Give the extent of all Trypanosoma brucei.
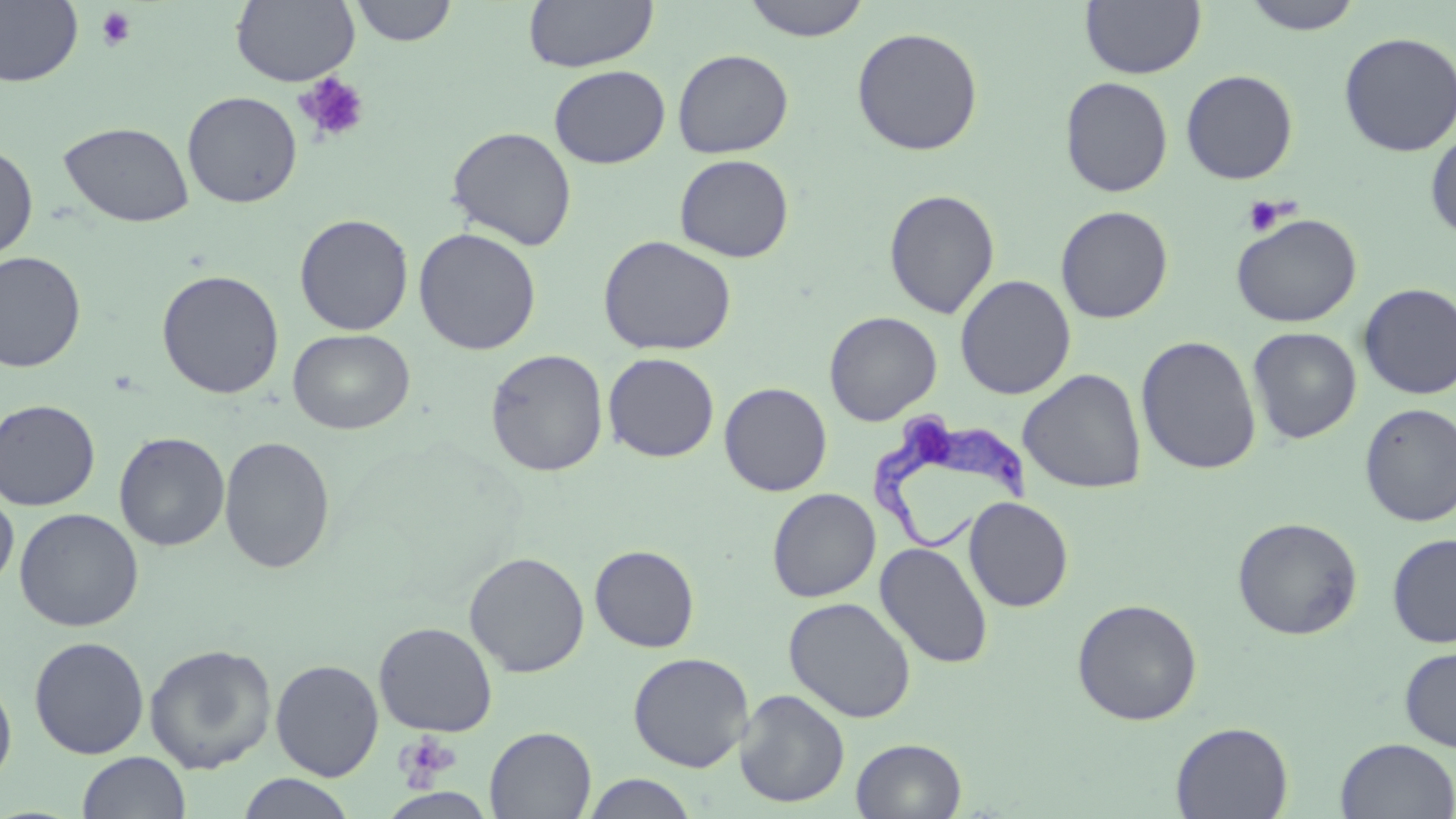
Approximate bounding boxes as (x1, y1, x2, y2) in pixels.
Trypanosoma brucei: (867, 413, 1041, 555).

Summary:
  - Uninfected red blood cell locations: (0, 0, 83, 87), (231, 0, 359, 86), (350, 0, 458, 46), (523, 0, 658, 73), (741, 0, 871, 41), (1079, 0, 1206, 79), (1239, 0, 1366, 35), (851, 26, 983, 156), (1338, 31, 1456, 157), (672, 49, 794, 159), (549, 65, 670, 168), (1180, 69, 1299, 184), (1060, 76, 1173, 197), (182, 91, 302, 208), (58, 121, 194, 228), (445, 126, 578, 250), (1425, 128, 1456, 241), (0, 143, 38, 262), (674, 153, 794, 263), (883, 188, 1000, 319), (1055, 205, 1173, 324), (294, 213, 414, 336), (1230, 213, 1362, 327), (413, 227, 542, 356), (597, 234, 736, 356), (0, 251, 87, 373), (156, 269, 285, 399), (955, 274, 1076, 400), (1357, 283, 1456, 399), (824, 311, 942, 425), (1247, 327, 1362, 444), (288, 328, 415, 435), (1136, 335, 1262, 475), (485, 348, 609, 477), (603, 352, 720, 462), (1018, 369, 1147, 493), (719, 382, 832, 496), (0, 399, 101, 511), (1359, 403, 1456, 527), (114, 432, 230, 551), (219, 435, 336, 575), (767, 488, 881, 602), (0, 489, 19, 592), (772, 489, 889, 720), (964, 496, 1074, 612), (14, 507, 144, 632), (1232, 517, 1363, 640), (1387, 533, 1456, 648), (875, 542, 993, 668), (589, 545, 699, 653), (464, 551, 589, 677), (783, 596, 917, 723), (1072, 598, 1202, 726), (373, 621, 498, 737), (29, 636, 150, 759), (144, 643, 277, 773), (1399, 646, 1456, 751), (628, 651, 754, 772), (270, 659, 384, 781), (0, 671, 17, 789), (734, 689, 850, 808), (1170, 721, 1293, 819), (485, 726, 597, 818), (1335, 737, 1456, 818), (851, 738, 967, 818), (76, 750, 191, 819), (235, 773, 356, 818), (582, 774, 699, 818)
  - Platelet locations: (94, 6, 137, 52), (294, 72, 371, 145), (1241, 196, 1289, 237), (396, 732, 461, 789)
  - Slide-level diagnosis: Trypanosoma brucei
  - Field of view: one of a larger specimen
  - Image size: 1456×819 pixels
  - Modality: light microscopy
  - Stain: May-Grünwald-Giemsa
  - Preparation: thin blood smear
  - Magnification: 1000x